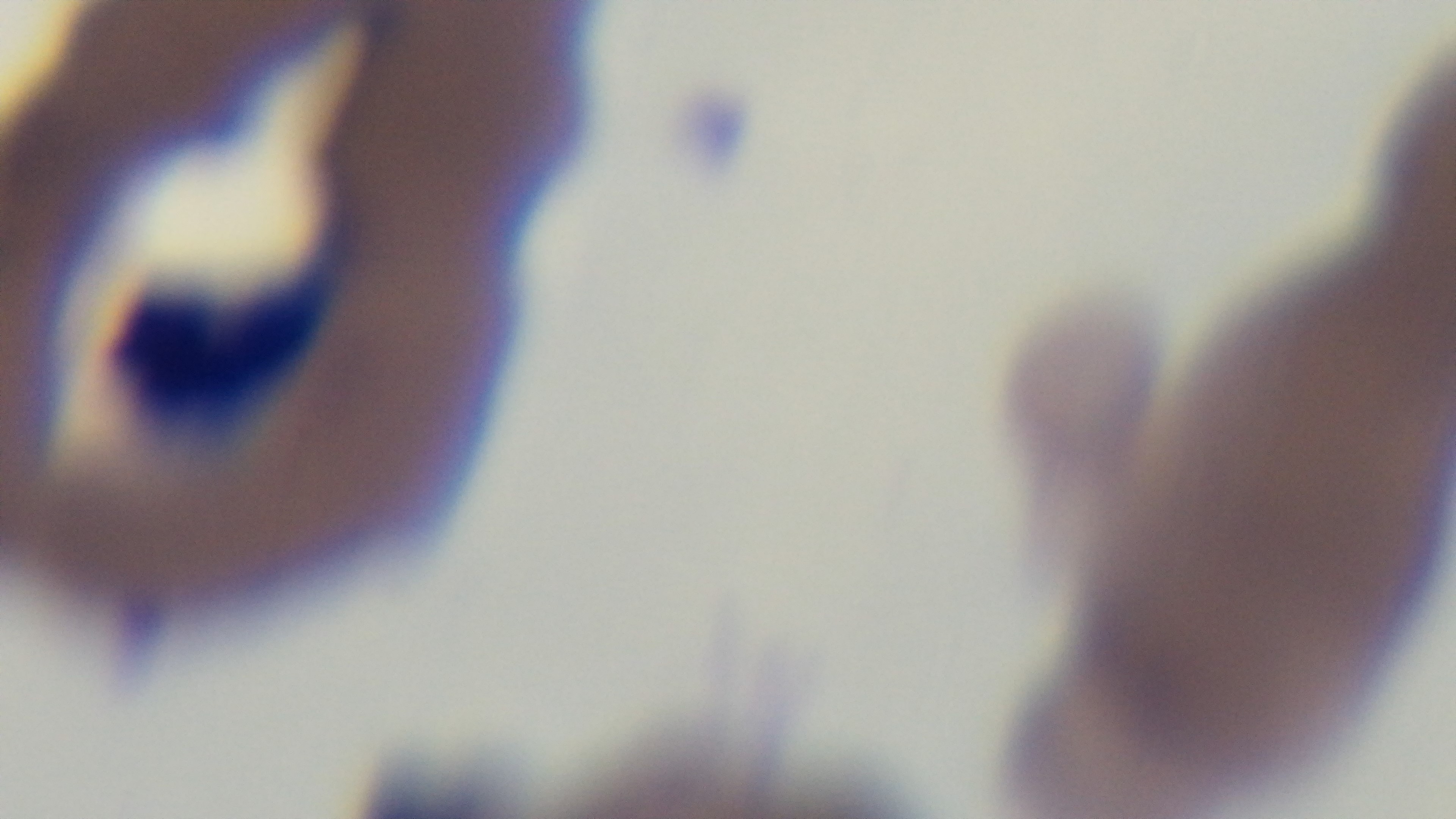

field of view = one from the slide
preparation = thin smear
malaria status = infected
modality = light microscopy
objective = 100x oil immersion
capture = mounted 4K digital camera
stain = Giemsa